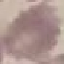
Summary:
  - Malaria status: uninfected
  - Preparation: thin smear
  - Capture: smartphone through the microscope eyepiece
  - Stain: Giemsa
  - Image type: cell patch, automatically extracted from a larger field of view and resized to 64 × 64 pixels